Classify this cell by malaria status.
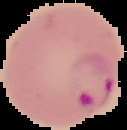

Parasitized.

Summary:
  - Image size: 127×130 pixels
  - Preparation: thin blood smear
  - Image type: segmented cell region with the area outside set to black